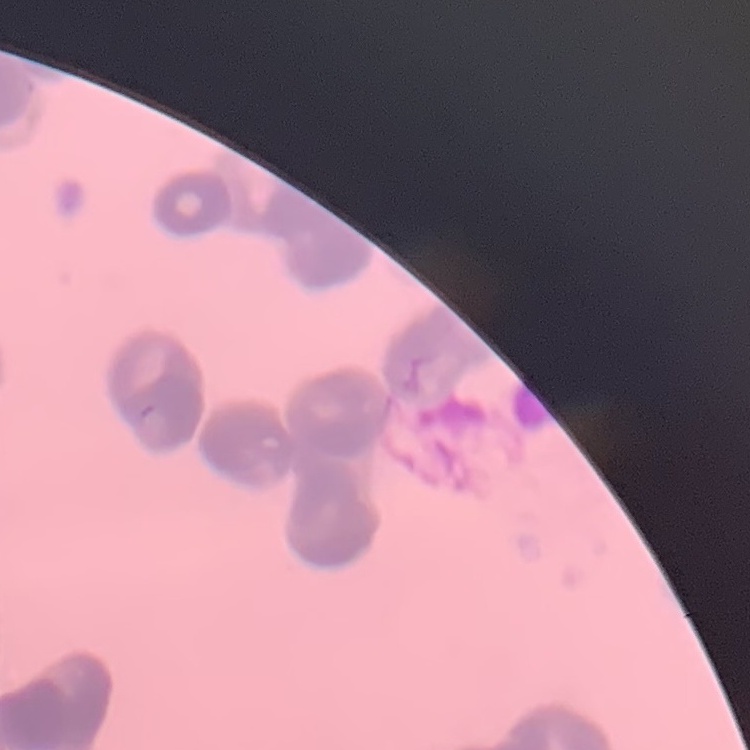 The red blood cells exhibit rouleaux formation. Stained with either Field's or Giemsa. Thin blood film. One tile cut from a larger photomicrograph.